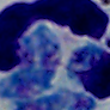
magnification = 1000x
identification = white blood cell
modality = photomicrograph